Identify the preparation type.
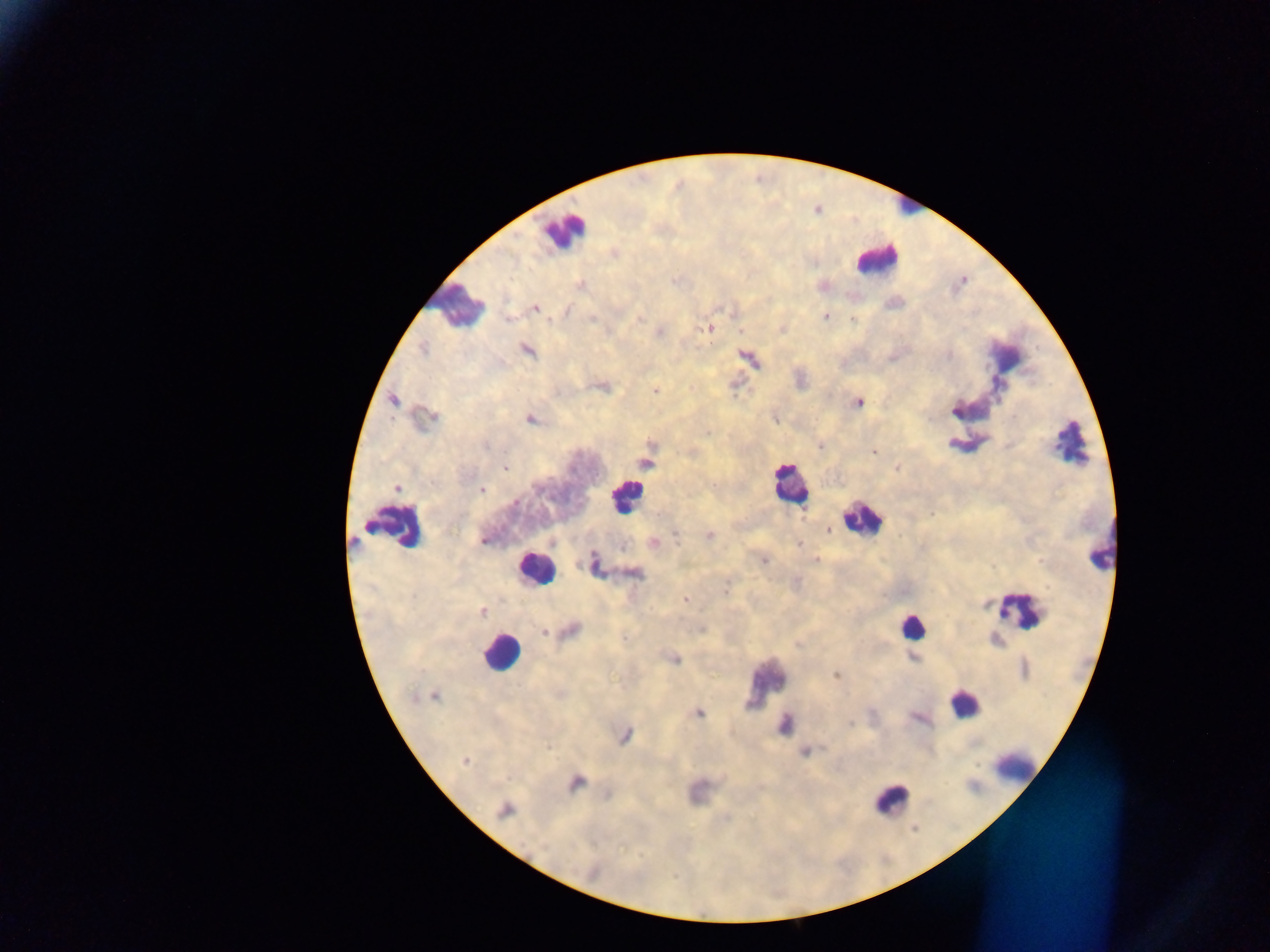
This is a thick smear.

Approximate centers as (x, y) in pixels. Leukocyte locations: (906, 202), (563, 230), (875, 258), (458, 304), (1070, 443), (790, 485), (624, 497), (862, 519), (398, 526), (1099, 553), (534, 568), (1019, 610), (912, 626), (500, 654), (765, 681), (964, 703), (1014, 765), (892, 799). Plasmodium parasite locations: (614, 254), (580, 286), (535, 308), (567, 312), (825, 316), (592, 318), (639, 318), (509, 319), (853, 319), (709, 328), (741, 331), (423, 349), (528, 351), (948, 355), (604, 387), (654, 391), (393, 400), (859, 402), (955, 410), (431, 417), (530, 419), (708, 433), (820, 446), (874, 452), (646, 464), (505, 468), (897, 468), (396, 489), (481, 490), (515, 502), (932, 513), (833, 534), (676, 535), (710, 536), (483, 541), (653, 542), (799, 544), (815, 560), (763, 561), (595, 564), (635, 573), (726, 590), (684, 600), (482, 611), (570, 630), (543, 633), (913, 657), (675, 658), (836, 675), (434, 696), (699, 713), (850, 723), (784, 725), (625, 736), (549, 747), (805, 752), (464, 762), (575, 782), (606, 795), (505, 811), (593, 872). Photographed through a microscope with a mobile-phone camera. Sample from Ghana. Image is 1270×952 pixels. Single field of view.